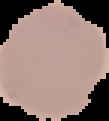
The area outside the segmented cell region is set to black. Image is 109×121 pixels. Result: no Plasmodium parasites detected. From a thin blood film.